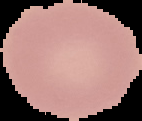

Summary:
  - Image size: 142×121 pixels
  - Malaria status: uninfected
  - Image type: segmented cell region on a black background
  - Preparation: thin blood film